Comment on the morphology of the red blood cells.
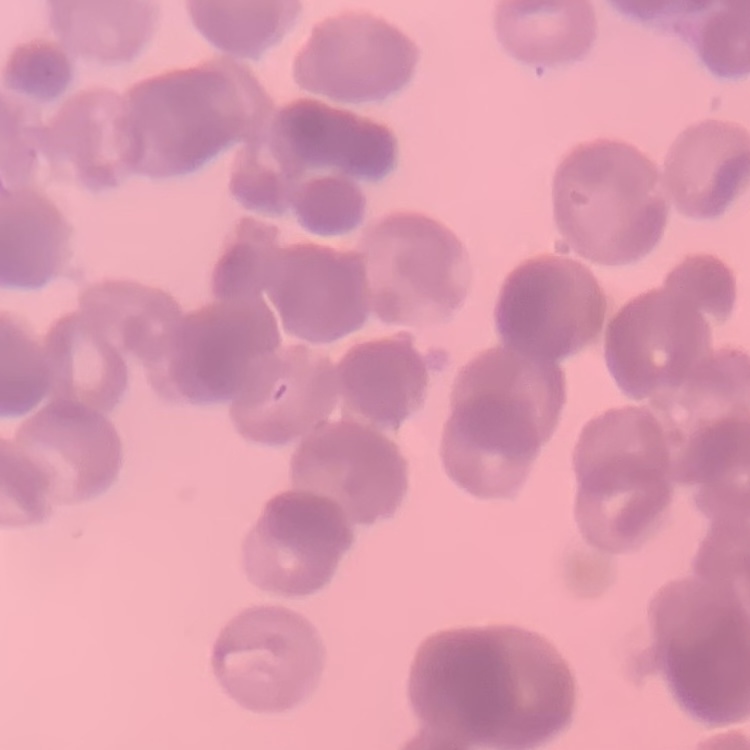

Rouleaux formation.

stain = Field's or Giemsa
preparation = thin blood film
image type = square crop of a larger photomicrograph